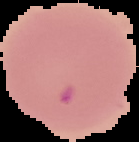 Result: no malaria parasites detected. Image is 139×142 pixels. The area outside the segmented cell region is set to black. From a thin blood smear.